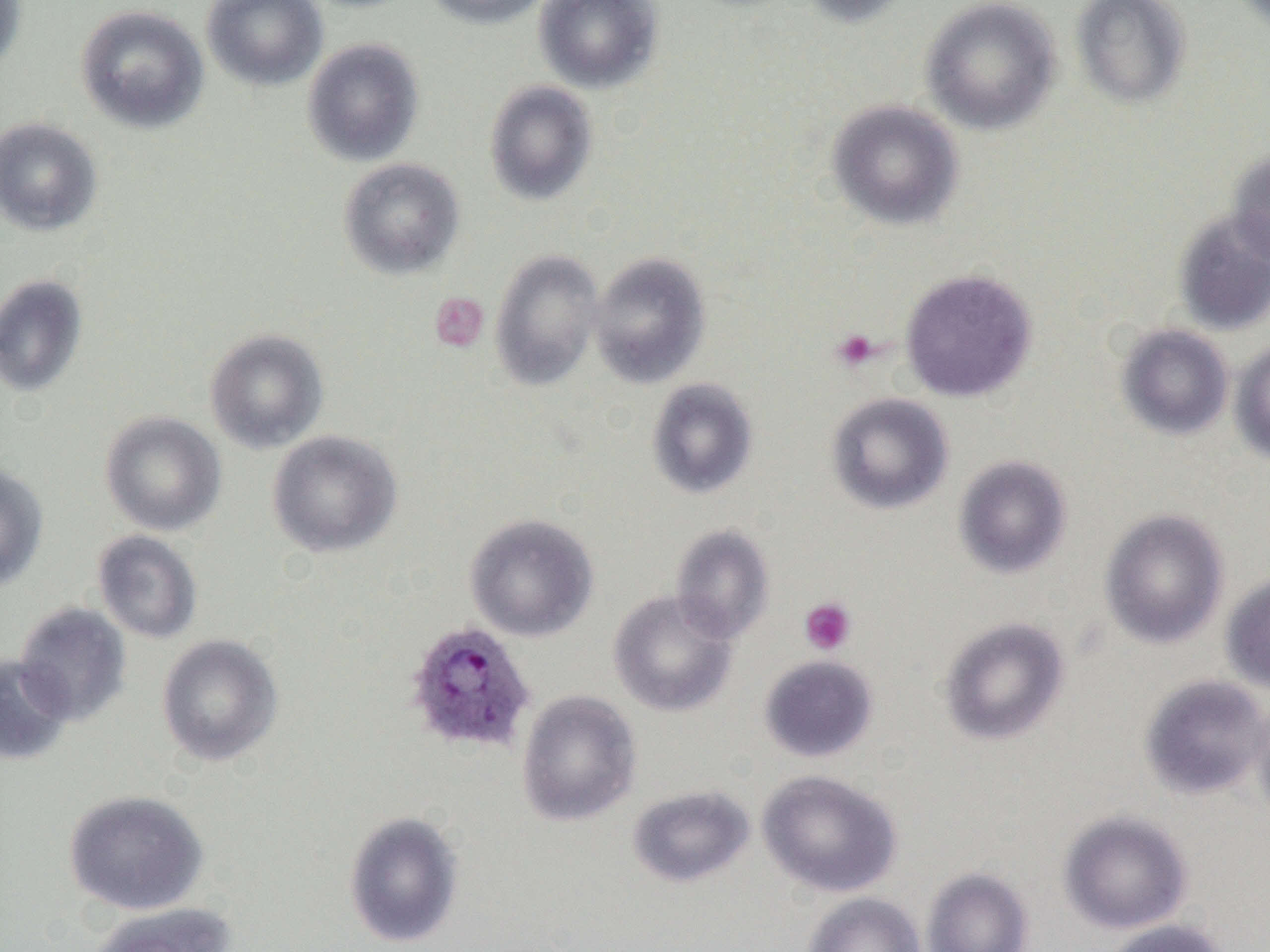

Plasmodium ovale-infected red blood cell locations = approximate bounding boxes as (x1,y1)-(x2,y2) corner pairs in pixels: (404,620)-(536,756)
slide-level diagnosis = Plasmodium ovale
image size = 1270×952 pixels
uninfected red blood cell locations = approximate bounding boxes as (x1,y1)-(x2,y2) corner pairs in pixels: (0,0)-(28,76), (202,0)-(328,91), (422,0)-(554,29), (534,0)-(664,93), (797,0)-(914,27), (920,0)-(1061,135), (1071,0)-(1193,108), (74,4)-(209,134), (302,38)-(425,167), (484,80)-(599,205), (826,99)-(964,230), (0,117)-(103,237), (1227,149)-(1270,266), (338,158)-(465,280), (1172,210)-(1270,336), (490,249)-(604,390), (589,252)-(711,389), (899,269)-(1037,403), (0,274)-(88,398), (1116,324)-(1233,440), (204,329)-(329,454), (1229,339)-(1270,466), (646,378)-(759,500), (825,392)-(954,515), (100,411)-(226,536), (267,430)-(403,558), (953,455)-(1072,579), (0,462)-(49,592), (1099,509)-(1229,649), (464,513)-(599,641), (670,524)-(775,643), (92,530)-(203,644), (1221,574)-(1270,695), (608,590)-(737,717), (15,602)-(132,726), (938,616)-(1070,746), (156,634)-(284,767), (0,654)-(73,766), (759,655)-(878,763), (1139,674)-(1269,800), (516,689)-(642,827), (1250,697)-(1270,826), (757,769)-(902,898), (627,784)-(755,888), (63,789)-(208,915), (343,810)-(465,948), (1059,810)-(1193,935), (921,866)-(1034,952), (802,891)-(926,952), (87,902)-(237,952), (1102,918)-(1232,952)
magnification = 1000x
modality = light microscopy
preparation = thin blood film
field of view = single
platelet locations = approximate bounding boxes as (x1,y1)-(x2,y2) corner pairs in pixels: (429,293)-(489,352), (831,329)-(882,371), (799,597)-(857,656)